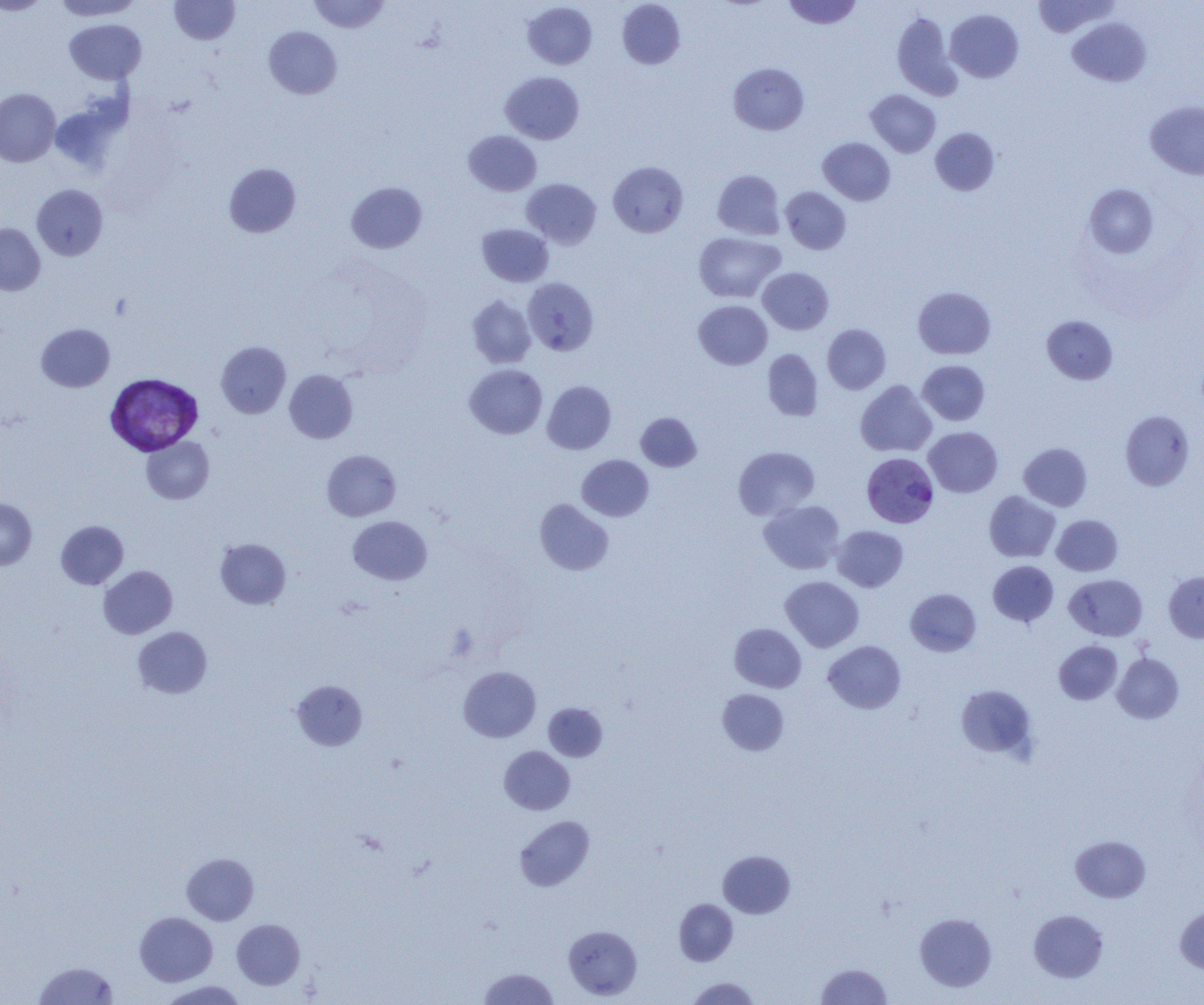 Approximate bounding boxes as (x1,y1)-(x2,y2) corner pairs in pixels. Plasmodium vivax-infected red blood cell locations: (105,373)-(203,456), (862,452)-(939,528). Uninfected red blood cell locations: (0,0)-(50,15), (52,0)-(143,21), (169,0)-(240,45), (307,0)-(390,33), (783,0)-(863,29), (1032,0)-(1118,38), (617,1)-(685,69), (523,2)-(597,69), (945,9)-(1024,83), (892,12)-(959,99), (1067,17)-(1151,86), (64,19)-(146,84), (264,26)-(342,99), (729,63)-(809,135), (500,71)-(584,144), (0,88)-(60,166), (866,90)-(940,157), (50,96)-(129,173), (1145,101)-(1204,180), (930,127)-(1000,195), (463,130)-(541,195), (818,137)-(895,205), (608,161)-(688,237), (224,163)-(301,237), (712,169)-(785,240), (522,178)-(601,248), (346,182)-(427,253), (31,184)-(108,260), (1083,184)-(1159,258), (780,186)-(851,254), (0,223)-(45,295), (477,223)-(553,286), (693,232)-(785,303), (758,267)-(833,334), (523,277)-(599,355), (913,287)-(995,359), (467,295)-(536,368), (694,300)-(772,369), (1041,315)-(1118,384), (36,323)-(115,392), (822,324)-(890,393), (216,342)-(291,418), (762,349)-(823,421), (917,360)-(990,425), (465,363)-(547,439), (284,369)-(357,443), (855,380)-(937,457), (543,381)-(616,454), (1120,410)-(1195,491), (636,412)-(702,472), (923,427)-(1003,497), (141,436)-(214,504), (1018,442)-(1092,511), (733,446)-(820,520), (322,450)-(401,521), (577,455)-(653,521), (984,491)-(1060,562), (0,497)-(37,570), (535,499)-(613,575), (759,499)-(845,574), (1051,514)-(1122,576), (348,515)-(432,585), (56,520)-(128,589), (832,526)-(908,592), (215,538)-(291,609), (988,561)-(1058,626), (99,565)-(177,638), (1164,571)-(1204,642), (1064,574)-(1148,641), (780,576)-(864,652), (905,588)-(981,656), (730,623)-(806,692), (133,626)-(212,698), (823,640)-(906,714), (1054,640)-(1122,705), (1112,653)-(1184,723), (458,666)-(541,742), (291,679)-(368,750), (955,684)-(1039,760), (717,688)-(789,755), (543,703)-(607,761), (499,746)-(574,815), (514,816)-(594,891), (1070,835)-(1150,902), (718,850)-(795,918), (181,853)-(259,925), (674,899)-(737,965), (1175,906)-(1204,973), (1029,909)-(1109,982), (134,911)-(217,986), (915,912)-(997,992), (231,919)-(305,989), (563,925)-(642,1000), (33,961)-(118,1005), (816,963)-(892,1005), (479,968)-(558,1004), (686,976)-(761,1005), (158,980)-(248,1005). Slide-level diagnosis: Plasmodium vivax. 1000x magnification. Thin blood film. Single field of view. Optical microscopy. Image is 1204×1005 pixels.